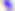 Micrograph. Captured at 400x magnification. Toxoplasma gondii is seen.